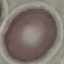

Summary:
  - Result: no malaria parasites seen
  - Capture: smartphone camera at the microscope eyepiece
  - Image type: automatically extracted cell patch, resized to 64 × 64 pixels
  - Preparation: thin blood smear
  - Stain: Giemsa